Evaluate for Plasmodium parasites.
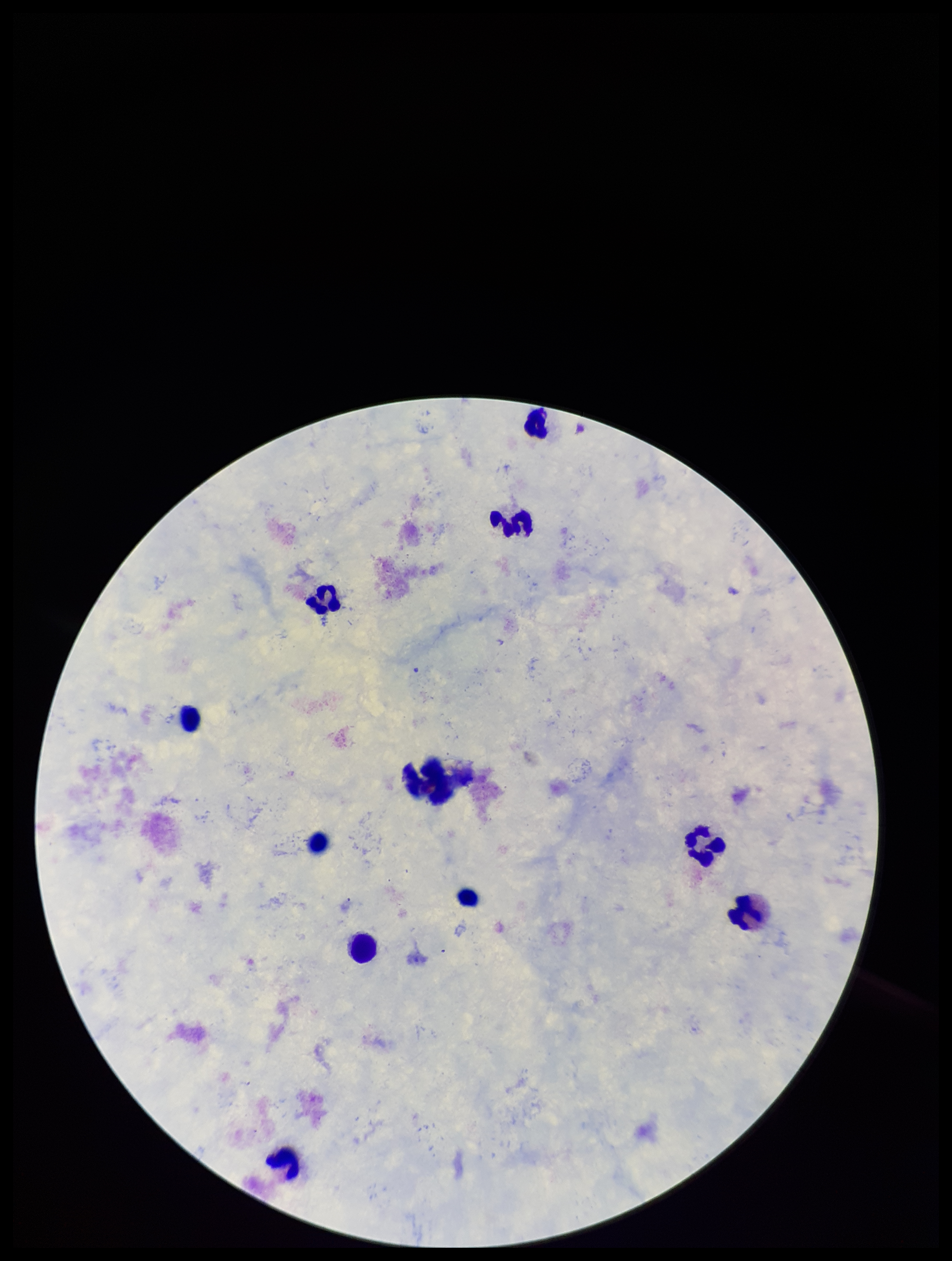

None seen.

image size = 952×1261 pixels
stain = Giemsa
field of view = one from this slide
preparation = thick smear
leukocyte count = 11
capture = smartphone photograph through the microscope eyepiece
patient malaria status = negative
parasite count = 0